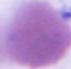
modality = photomicrograph
identification = red blood cell
magnification = 1000x